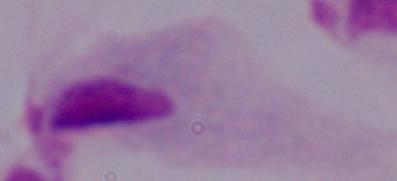

A trichomonad is shown. Micrograph. Captured at 1000x magnification.